Identify the parasite.
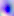
This is Toxoplasma gondii.

{
  "modality": "micrograph",
  "magnification": "400x"
}